Locate every malaria parasite.
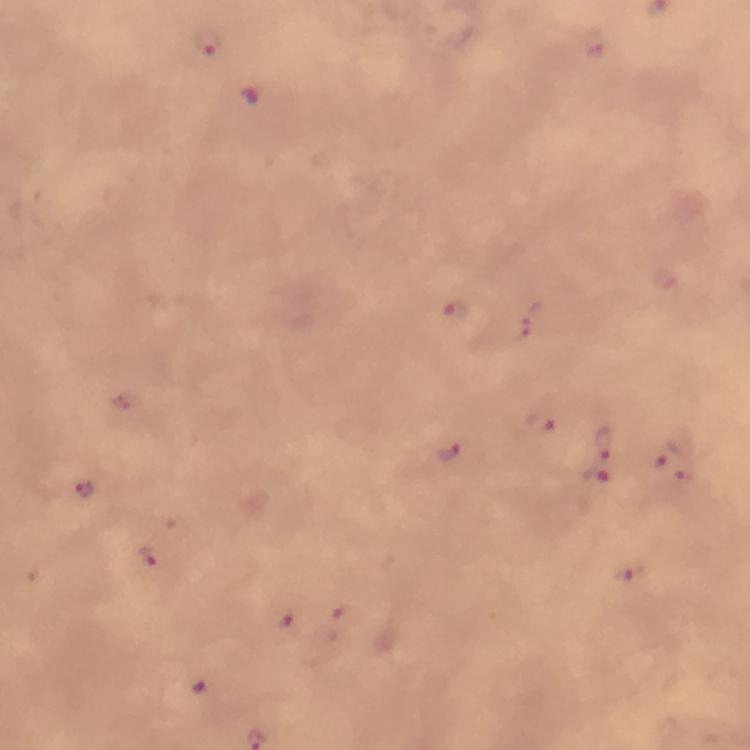

Approximate object centers, in pixels from the top-left corner.
Malaria parasites: (x=595, y=43), (x=208, y=45), (x=449, y=314), (x=529, y=319), (x=541, y=424), (x=601, y=441), (x=446, y=451), (x=659, y=455), (x=681, y=466), (x=592, y=477), (x=87, y=493), (x=151, y=554), (x=286, y=624).

From a malaria diagnostic workup. Thick blood film. Giemsa-stained preparation. Image is 750×750 pixels. A crop from one field of view. Immersion oil was used. Smartphone photograph taken through a microscope. At 100x magnification.